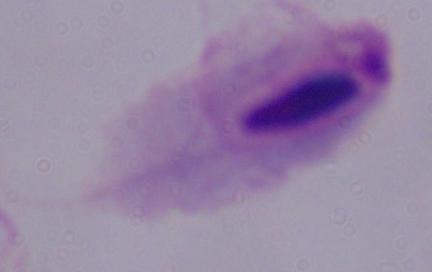 1000x magnification. Photomicrograph. A trichomonad is shown.